Describe the morphology of the erythrocytes.
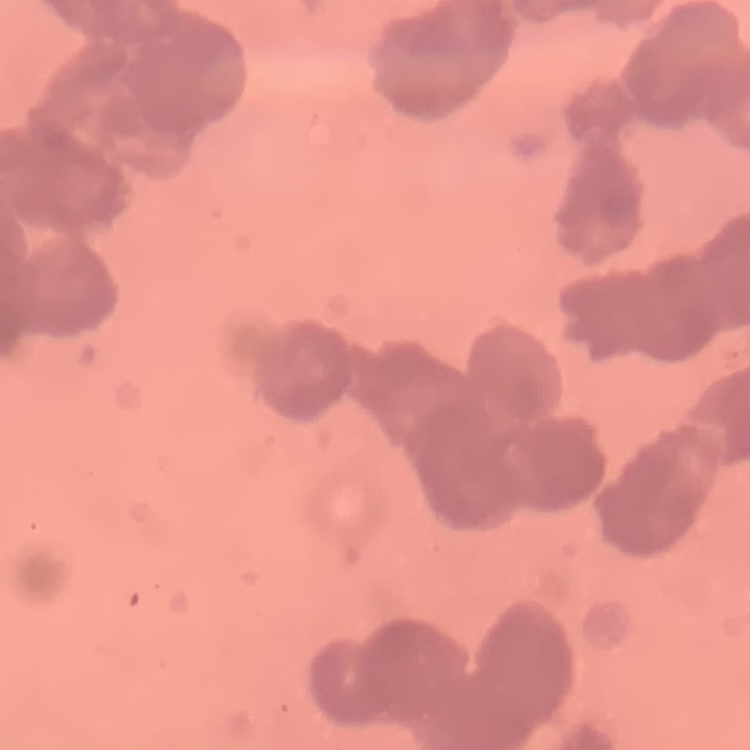
They show rouleaux formation.

Summary:
  - Stain: Field's or Giemsa
  - Preparation: thin blood smear
  - Image type: one tile cut from a larger photomicrograph